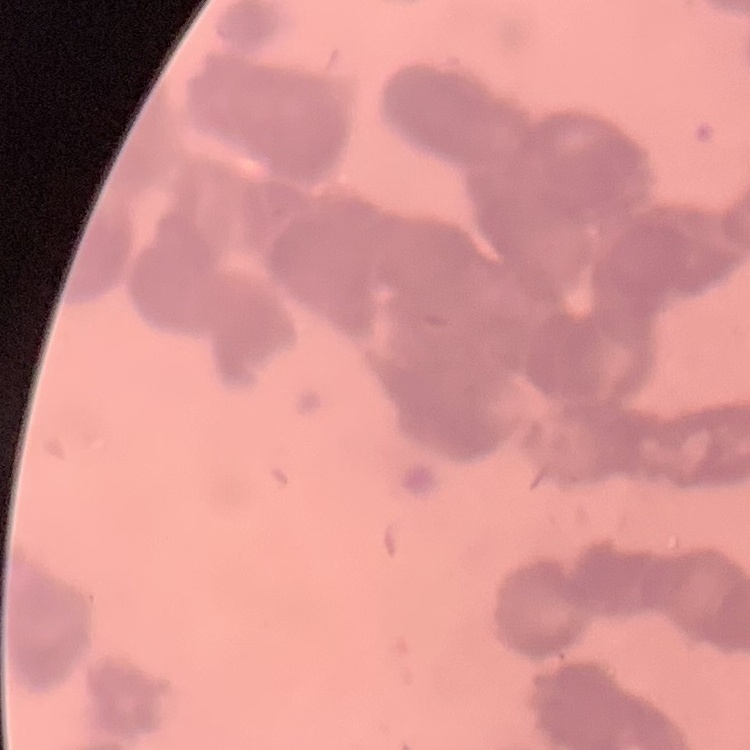

Summary:
  - Erythrocyte morphology: rouleaux formation
  - Preparation: thin blood smear
  - Stain: Field's or Giemsa
  - Image type: square crop of a larger photomicrograph